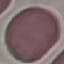
{
  "result": "no malaria parasites seen",
  "preparation": "thin smear",
  "stain": "Giemsa",
  "image_type": "automatically extracted cell patch, resized to 64 × 64 pixels",
  "capture": "smartphone through the microscope eyepiece"
}